Report the malaria status of this cell.
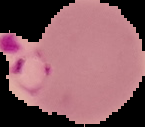

Parasitized.

From a thin blood film. Segmented cell region on a black background. Image is 145×127 pixels.